Evaluate for malaria.
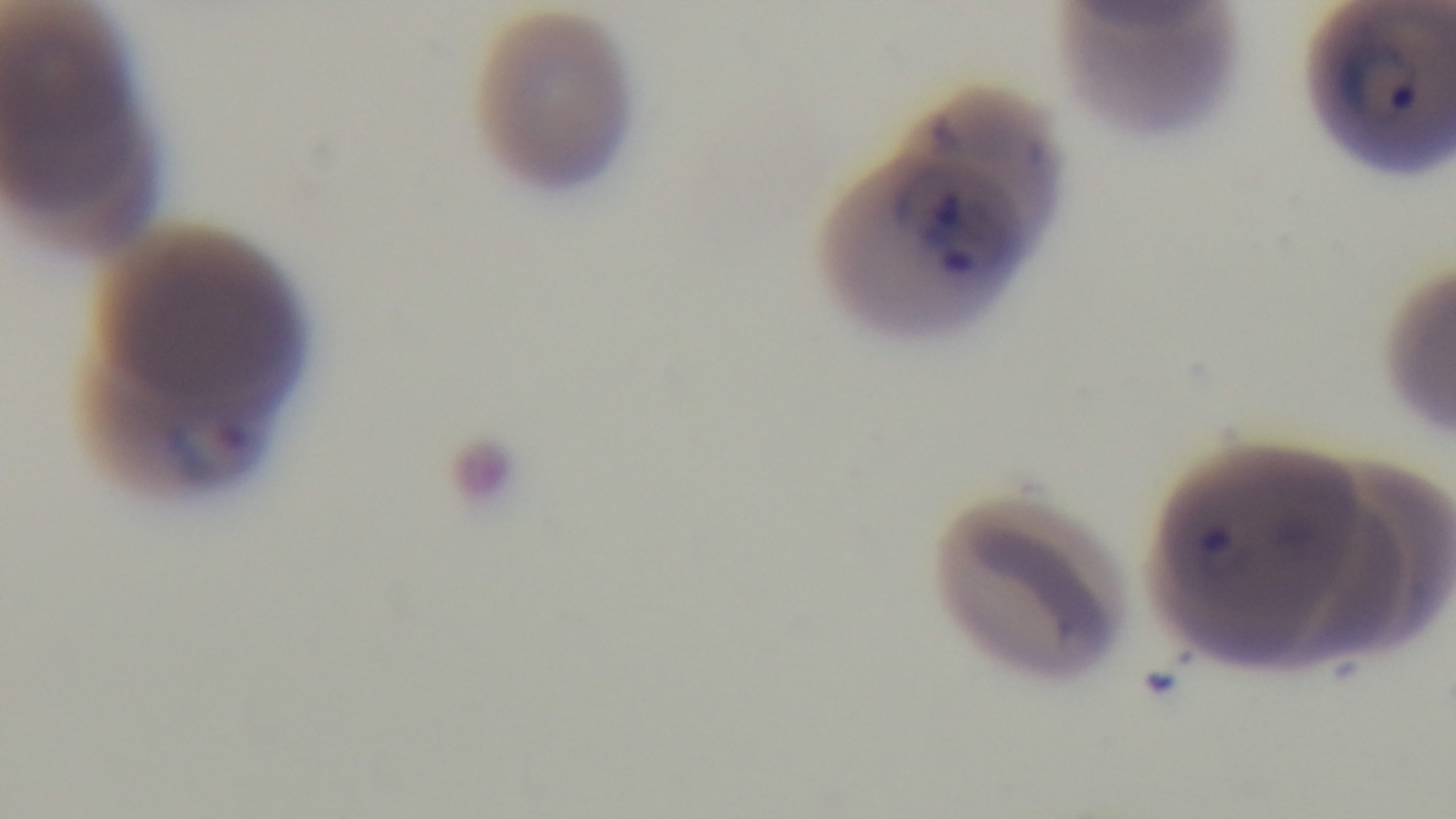

It is infected.

Mounted 4K digital camera. Photomicrograph. Oil-immersion objective, 100x. Preparation: thin. Giemsa-stained. Single field of view.